Classify this cell by malaria status.
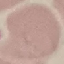
Uninfected.

capture = smartphone through the microscope eyepiece
image type = cell patch, automatically extracted from a larger field of view and resized to 64 × 64 pixels
stain = Giemsa
preparation = thin blood smear